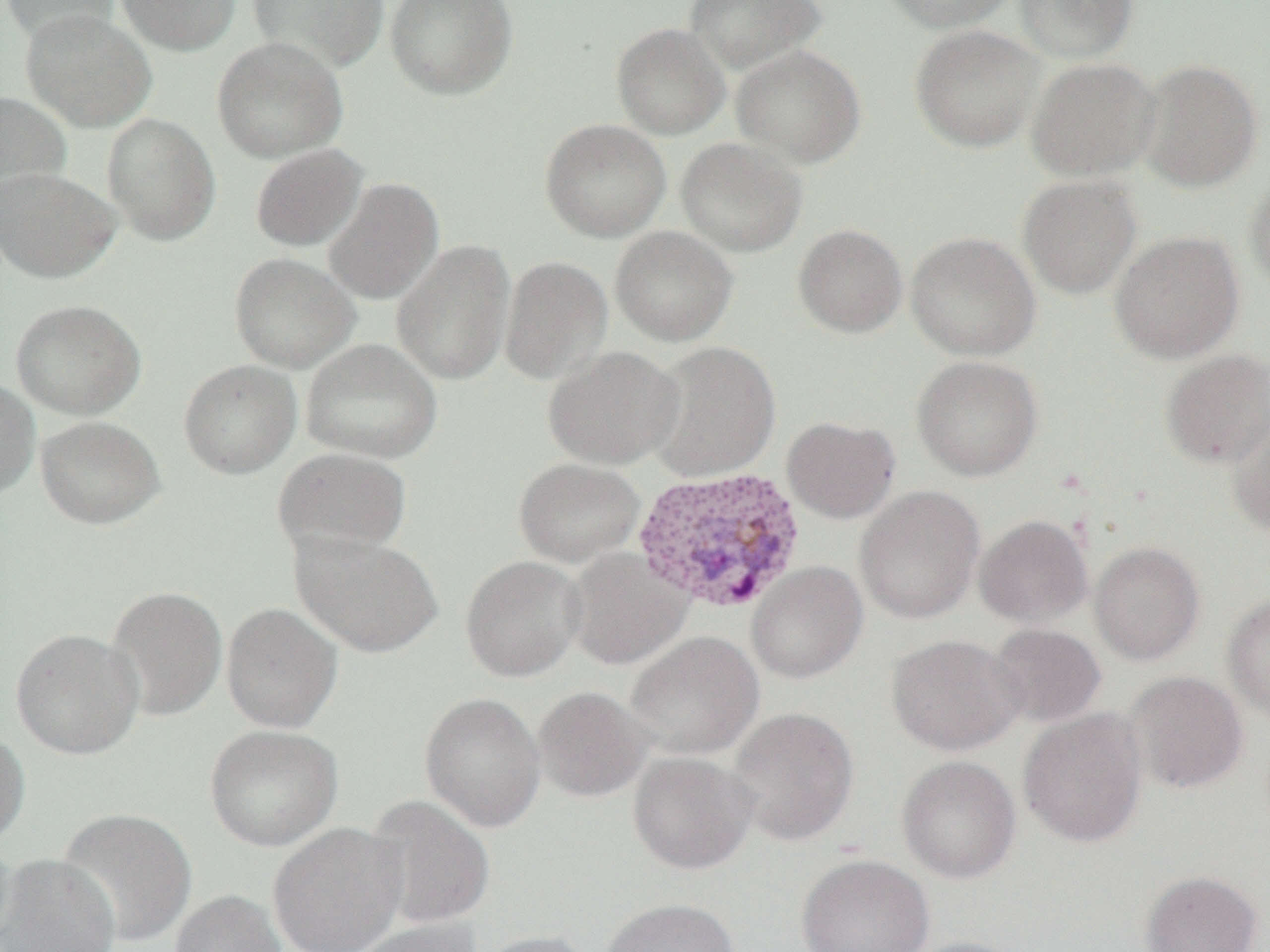
Summary:
  - Coordinate format: approximate bounding boxes as (x1, y1, x2, y2) in pixels
  - Plasmodium vivax-infected red blood cell locations: (632, 465, 806, 614)
  - Uninfected red blood cell locations: (116, 0, 241, 56), (247, 0, 389, 75), (384, 0, 518, 100), (683, 0, 827, 74), (879, 0, 1019, 33), (1014, 0, 1138, 63), (1, 1, 120, 46), (21, 8, 157, 132), (611, 22, 730, 140), (910, 24, 1044, 153), (212, 36, 349, 162), (731, 44, 866, 169), (1026, 57, 1161, 181), (1136, 59, 1262, 192), (0, 91, 71, 209), (102, 113, 221, 244), (540, 119, 671, 242), (676, 137, 808, 257), (250, 144, 367, 252), (0, 167, 121, 283), (1245, 173, 1270, 293), (1017, 175, 1142, 300), (323, 177, 444, 305), (793, 223, 907, 338), (609, 226, 738, 347), (1109, 230, 1245, 363), (905, 231, 1040, 360), (392, 240, 515, 385), (229, 252, 360, 372), (499, 255, 613, 386), (10, 299, 146, 420), (300, 338, 443, 464), (646, 341, 780, 482), (544, 346, 684, 470), (1160, 348, 1270, 469), (911, 355, 1043, 481), (179, 359, 302, 479), (0, 377, 40, 501), (1227, 414, 1270, 536), (35, 415, 165, 529), (782, 416, 900, 523), (273, 447, 412, 557), (513, 458, 645, 568), (853, 485, 985, 624), (974, 514, 1093, 627), (290, 530, 444, 658), (1090, 542, 1205, 665), (563, 547, 693, 670), (460, 555, 587, 682), (746, 562, 868, 683), (104, 585, 227, 722), (1222, 594, 1270, 723), (221, 602, 343, 733), (987, 624, 1106, 727), (10, 628, 143, 760), (625, 631, 763, 759), (887, 634, 1026, 755), (1124, 670, 1249, 794), (533, 686, 652, 803), (420, 692, 546, 833), (728, 706, 859, 846), (1018, 708, 1149, 848), (205, 724, 342, 852), (0, 726, 30, 850), (627, 751, 758, 874), (897, 755, 1021, 883), (364, 795, 495, 929), (56, 807, 197, 948), (266, 822, 408, 952), (1, 854, 120, 951), (796, 854, 934, 952), (1139, 870, 1263, 952), (169, 890, 287, 952), (601, 898, 740, 952), (349, 918, 481, 952), (473, 930, 598, 952), (897, 937, 1028, 952)
  - Slide-level diagnosis: Plasmodium vivax
  - Field of view: single
  - Preparation: thin blood film
  - Modality: light microscopy
  - Image size: 1270×952 pixels
  - Magnification: 1000x